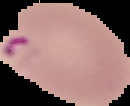
Summary:
  - Image type: segmented cell region with the area outside set to black
  - Malaria status: parasitized
  - Image size: 130×106 pixels
  - Preparation: thin blood film